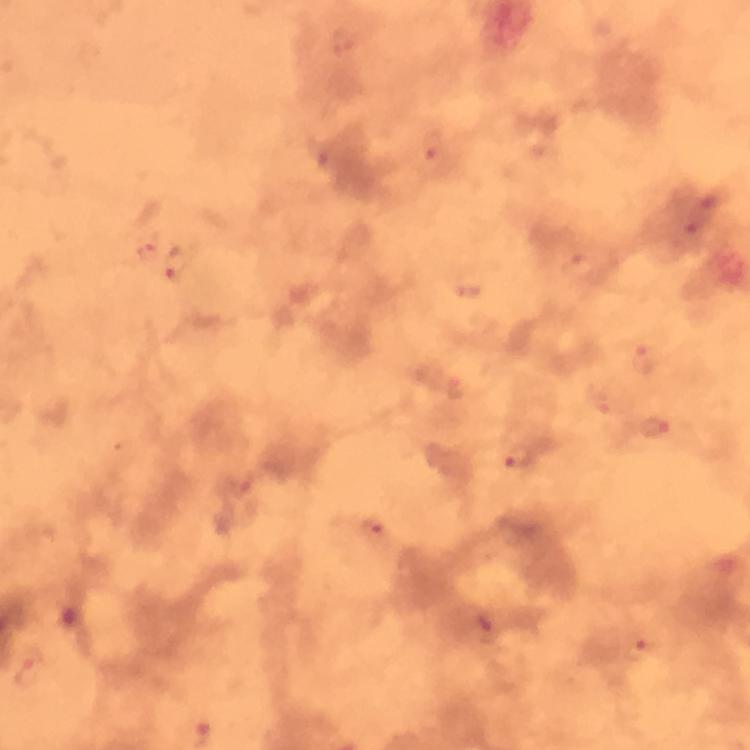
{
  "magnification": "100x",
  "cropped_from": "a single field of view",
  "plasmodium_parasite_locations": "approximate centers as {x, y} in pixels: {435, 160}, {149, 254}, {179, 264}, {579, 268}, {645, 356}, {654, 427}, {516, 455}, {372, 530}, {642, 648}, {31, 672}",
  "preparation": "thick blood film",
  "stain": "Giemsa",
  "capture": "smartphone camera through the microscope",
  "image_size": "750×750 pixels",
  "immersion_oil": "applied",
  "context": "from a malaria diagnostic workup"
}